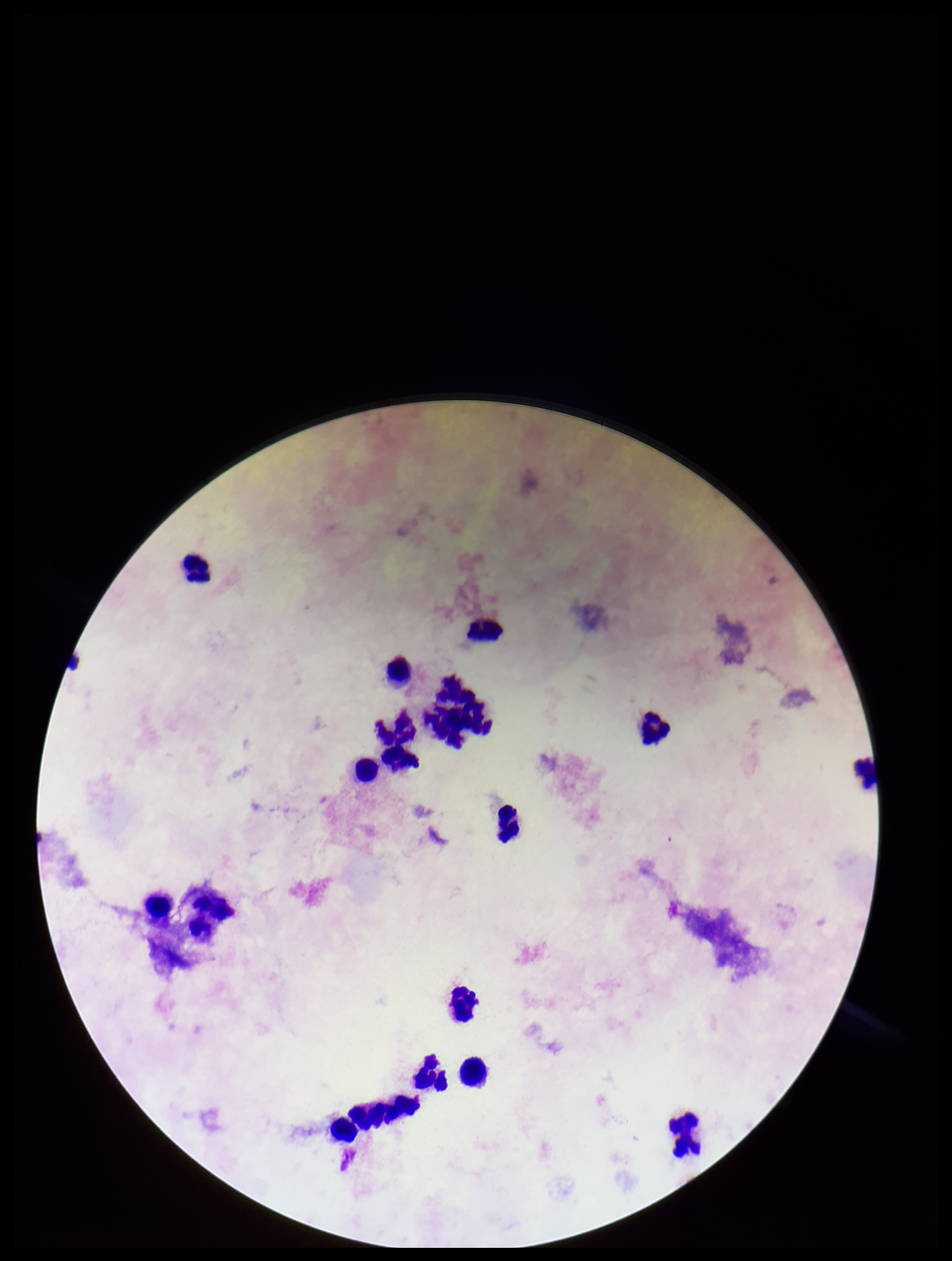

Image is 952×1261 pixels. Leukocyte count: 18. Photographed through the microscope eyepiece with a smartphone camera. Stained with Giemsa. Patient malaria status: negative. One field from this slide. Preparation: thick. Parasite count: 0. Plasmodium parasites: none identified.